Give the position of every Plasmodium parasite.
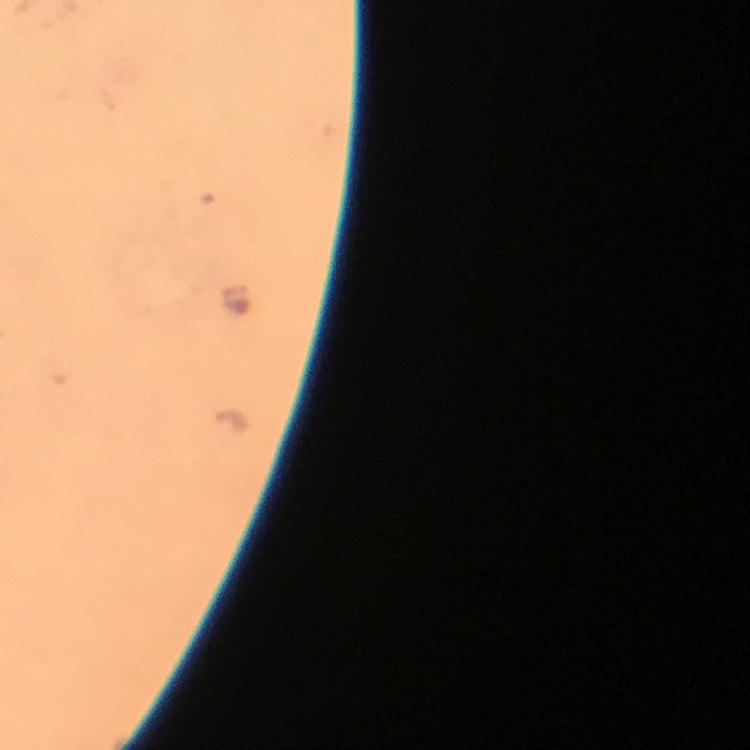

Approximate centers as (x, y) in pixels.
Plasmodium parasites: (235, 297).

Photographed through the microscope with a smartphone camera. Thick blood film. Immersion oil applied. At 100x magnification. From a diagnostic examination for malaria. Image is 750×750 pixels. Giemsa stain. A crop from one field of view.